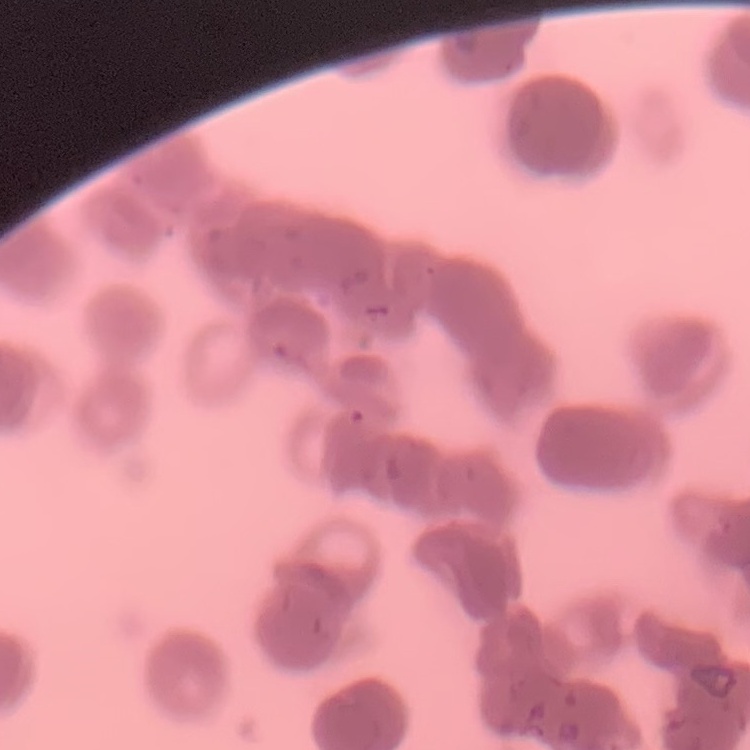 The red blood cells exhibit rouleaux formation. Stained with either Field's or Giemsa. Thin blood film. One tile cut from a larger photomicrograph.